Name the parasite shown.
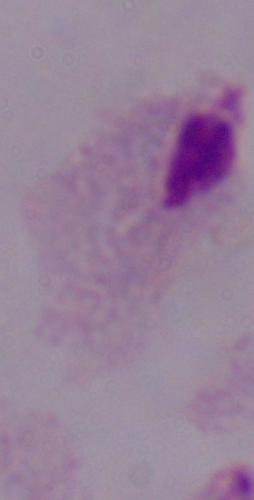
A trichomonad.

Summary:
  - Modality: photomicrograph
  - Magnification: 1000x